Locate and identify every blood parasite.
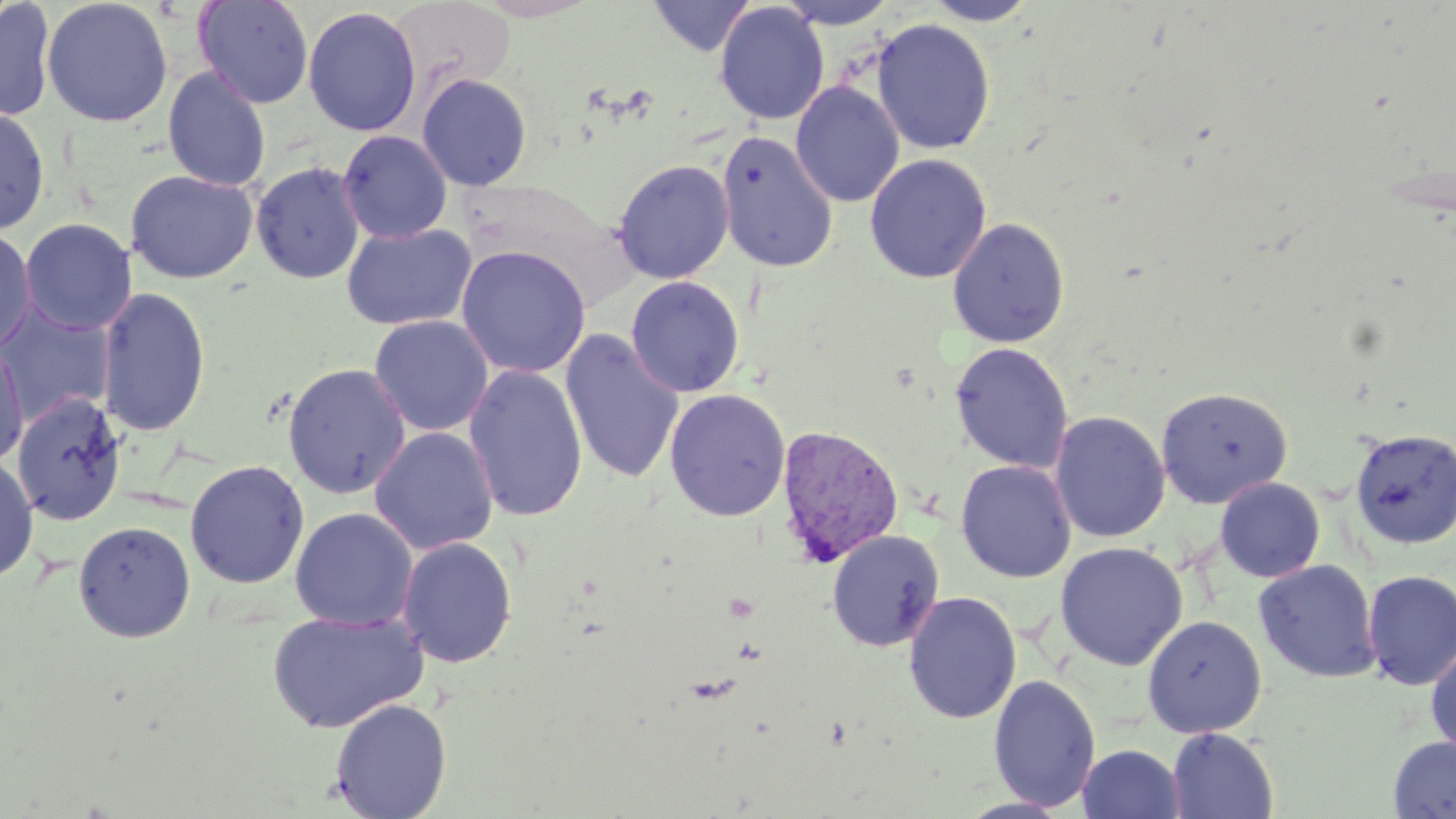

Approximate bounding boxes as (x1,y1)-(x2,y2) corner pairs in pixels.
Plasmodium vivax-infected red blood cells: (775,424)-(905,568).
No Plasmodium falciparum, Plasmodium ovale, Plasmodium malariae, Babesia divergens, or Trypanosoma brucei observed.

Uninfected red blood cell locations: (41,0)-(174,127), (193,0)-(315,109), (647,0)-(756,57), (776,0)-(899,29), (922,0)-(1041,25), (0,1)-(57,122), (714,3)-(829,125), (302,6)-(422,137), (871,19)-(996,155), (162,66)-(271,192), (417,73)-(532,191), (790,81)-(904,208), (0,106)-(51,235), (338,130)-(452,243), (716,131)-(838,273), (865,154)-(991,284), (612,159)-(734,284), (250,161)-(365,284), (125,169)-(259,284), (947,217)-(1070,348), (20,218)-(136,335), (341,222)-(477,331), (0,225)-(37,355), (455,246)-(591,379), (626,277)-(744,397), (96,285)-(211,437), (0,301)-(115,425), (369,315)-(494,437), (559,331)-(685,484), (1,341)-(29,468), (949,341)-(1074,474), (282,362)-(411,499), (463,364)-(588,523), (1155,386)-(1292,508), (664,389)-(791,521), (12,393)-(125,526), (1050,411)-(1170,543), (370,427)-(498,555), (1350,428)-(1456,549), (0,455)-(39,583), (185,459)-(310,589), (955,460)-(1076,583), (1214,477)-(1325,583), (290,507)-(418,631), (72,519)-(196,643), (827,530)-(944,652), (396,536)-(518,668), (1055,542)-(1188,671), (1253,559)-(1381,683), (1361,569)-(1456,690), (903,592)-(1021,724), (266,609)-(429,733), (1142,614)-(1267,738), (1426,640)-(1456,761), (987,674)-(1101,812), (329,698)-(452,819), (1167,727)-(1279,819), (1388,735)-(1456,818), (1078,744)-(1185,819). Slide-level diagnosis: Plasmodium vivax. Thin blood smear. Light microscopy. Image is 1456×819 pixels. Single field of view. Captured at 1000x magnification. May-Grünwald-Giemsa stain.